Identify the parasite.
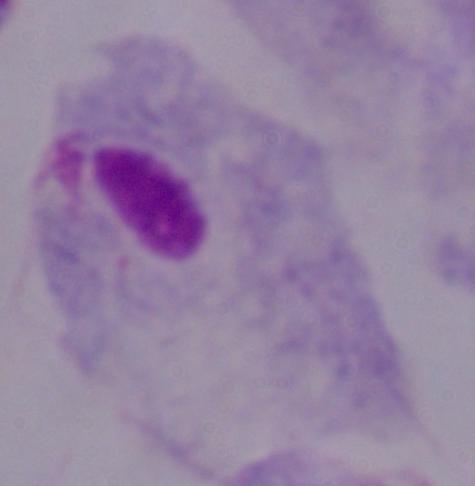
A trichomonad.

{
  "magnification": "1000x",
  "modality": "micrograph"
}